Assess for malaria.
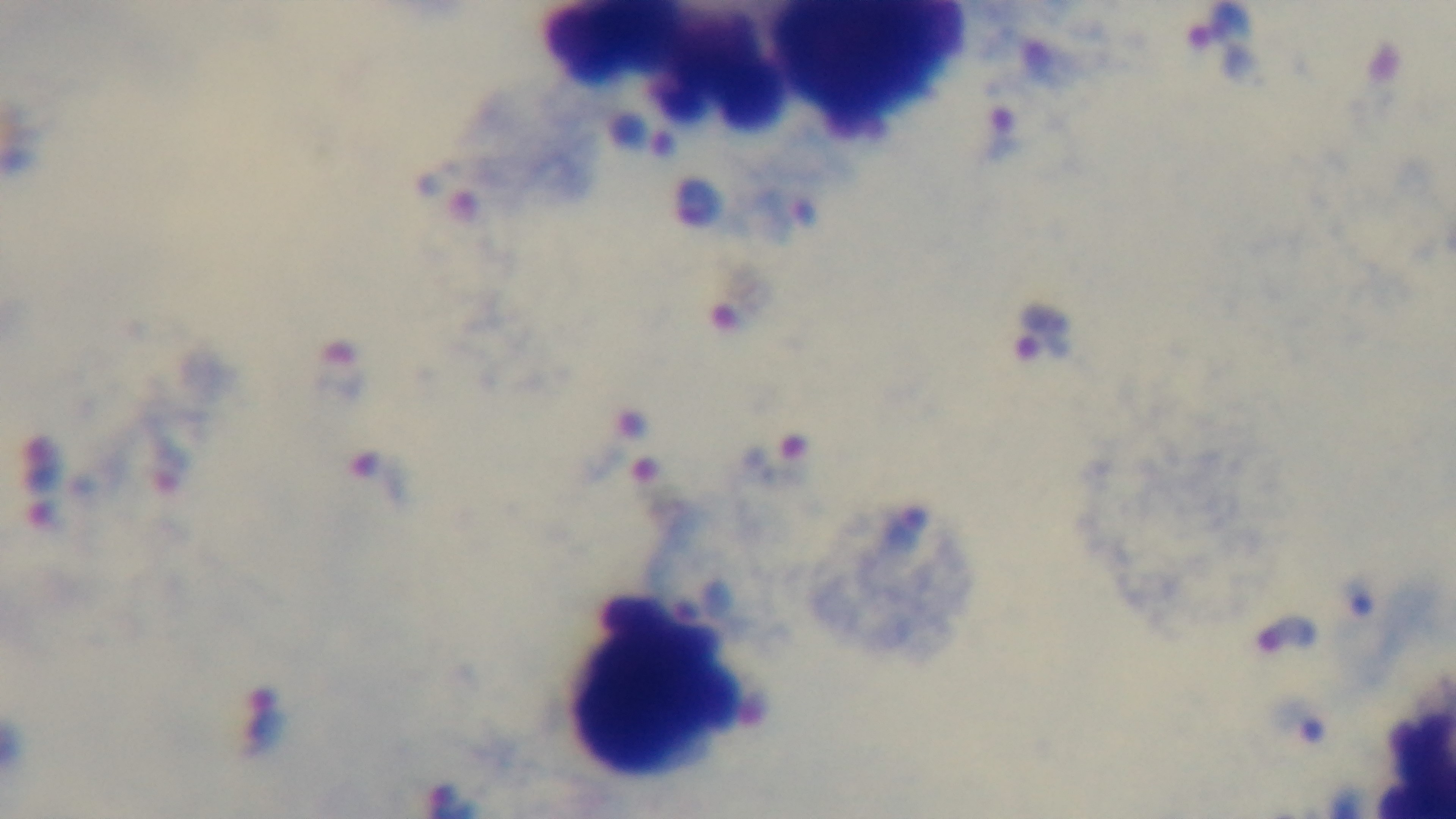

Positive.

Single field of view. Light microscopy. 100x oil-immersion objective. Preparation: thick smear. Captured with a mounted 4K digital camera. Giemsa stain.